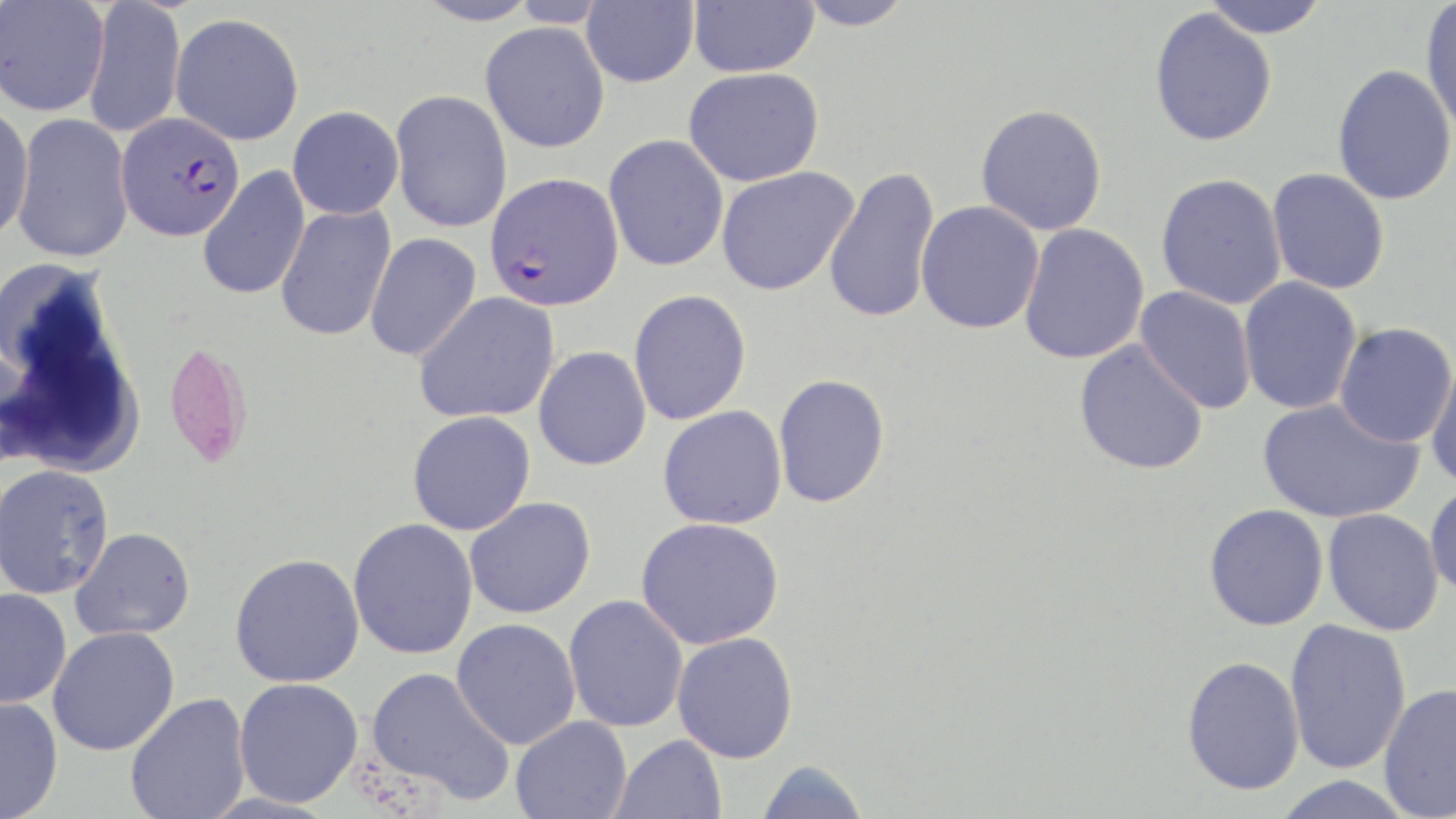
slide-level diagnosis = Plasmodium falciparum
magnification = 1000x
image size = 1456×819 pixels
stain = May-Grünwald-Giemsa
modality = optical microscopy
field of view = one of a larger specimen
uninfected red blood cell locations = approximate bounding boxes as named x1/y1/x2/y2 corners in pixels: (x1=1, y1=0, x2=109, y2=116), (x1=83, y1=0, x2=186, y2=139), (x1=411, y1=0, x2=540, y2=26), (x1=581, y1=0, x2=698, y2=88), (x1=689, y1=0, x2=819, y2=77), (x1=794, y1=0, x2=916, y2=30), (x1=1201, y1=0, x2=1331, y2=39), (x1=1421, y1=1, x2=1456, y2=139), (x1=1149, y1=7, x2=1278, y2=146), (x1=170, y1=13, x2=304, y2=146), (x1=480, y1=22, x2=610, y2=153), (x1=1332, y1=64, x2=1456, y2=205), (x1=683, y1=67, x2=824, y2=187), (x1=390, y1=89, x2=512, y2=233), (x1=975, y1=103, x2=1108, y2=236), (x1=0, y1=104, x2=34, y2=245), (x1=288, y1=105, x2=404, y2=219), (x1=11, y1=113, x2=136, y2=263), (x1=604, y1=135, x2=729, y2=271), (x1=197, y1=166, x2=311, y2=300), (x1=716, y1=166, x2=859, y2=296), (x1=824, y1=166, x2=941, y2=324), (x1=1266, y1=168, x2=1390, y2=295), (x1=1156, y1=173, x2=1287, y2=309), (x1=915, y1=200, x2=1044, y2=334), (x1=275, y1=205, x2=396, y2=341), (x1=1018, y1=223, x2=1150, y2=365), (x1=364, y1=232, x2=482, y2=362), (x1=1238, y1=276, x2=1363, y2=415), (x1=1134, y1=286, x2=1257, y2=414), (x1=628, y1=289, x2=752, y2=426), (x1=413, y1=292, x2=560, y2=424), (x1=1334, y1=322, x2=1456, y2=448), (x1=1073, y1=339, x2=1209, y2=475), (x1=163, y1=341, x2=252, y2=468), (x1=533, y1=346, x2=652, y2=471), (x1=1425, y1=353, x2=1456, y2=491), (x1=773, y1=373, x2=890, y2=508), (x1=1257, y1=397, x2=1422, y2=524), (x1=658, y1=405, x2=787, y2=530), (x1=407, y1=410, x2=536, y2=535), (x1=0, y1=463, x2=115, y2=599), (x1=1424, y1=481, x2=1456, y2=600), (x1=464, y1=497, x2=596, y2=618), (x1=1204, y1=504, x2=1329, y2=631), (x1=1323, y1=508, x2=1444, y2=635), (x1=636, y1=517, x2=785, y2=649), (x1=348, y1=518, x2=479, y2=659), (x1=71, y1=527, x2=196, y2=641), (x1=230, y1=552, x2=365, y2=688), (x1=0, y1=588, x2=72, y2=709), (x1=563, y1=594, x2=688, y2=733), (x1=451, y1=618, x2=581, y2=750), (x1=1284, y1=618, x2=1412, y2=774), (x1=48, y1=626, x2=180, y2=756), (x1=672, y1=632, x2=799, y2=764), (x1=1181, y1=655, x2=1305, y2=795), (x1=366, y1=666, x2=514, y2=806), (x1=234, y1=678, x2=363, y2=808), (x1=1379, y1=682, x2=1456, y2=818), (x1=125, y1=692, x2=251, y2=819), (x1=0, y1=697, x2=63, y2=819), (x1=510, y1=716, x2=632, y2=819), (x1=610, y1=734, x2=727, y2=819), (x1=755, y1=759, x2=870, y2=819), (x1=1269, y1=776, x2=1417, y2=819)
preparation = thin blood film
Plasmodium falciparum-infected red blood cell locations = approximate bounding boxes as named x1/y1/x2/y2 corners in pixels: (x1=116, y1=112, x2=245, y2=241), (x1=485, y1=172, x2=623, y2=312)